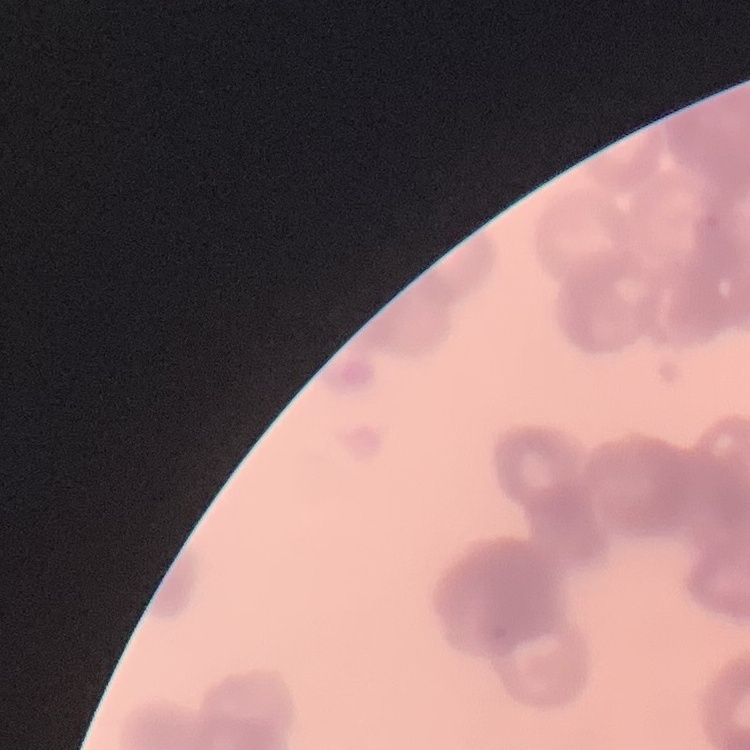

erythrocyte morphology = rouleaux formation
preparation = thin blood smear
stain = Field's or Giemsa
image type = square crop of a larger photomicrograph